Report the malaria status of this cell.
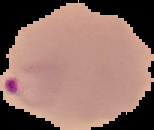

It is parasitized.

Summary:
  - Preparation: thin blood film
  - Image type: segmented cell region on a black background
  - Image size: 154×130 pixels